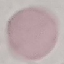
Summary:
  - Malaria status: uninfected
  - Preparation: thin blood film
  - Stain: Giemsa
  - Image type: automatically extracted cell patch, resized to 64 × 64 pixels
  - Capture: smartphone through the microscope eyepiece